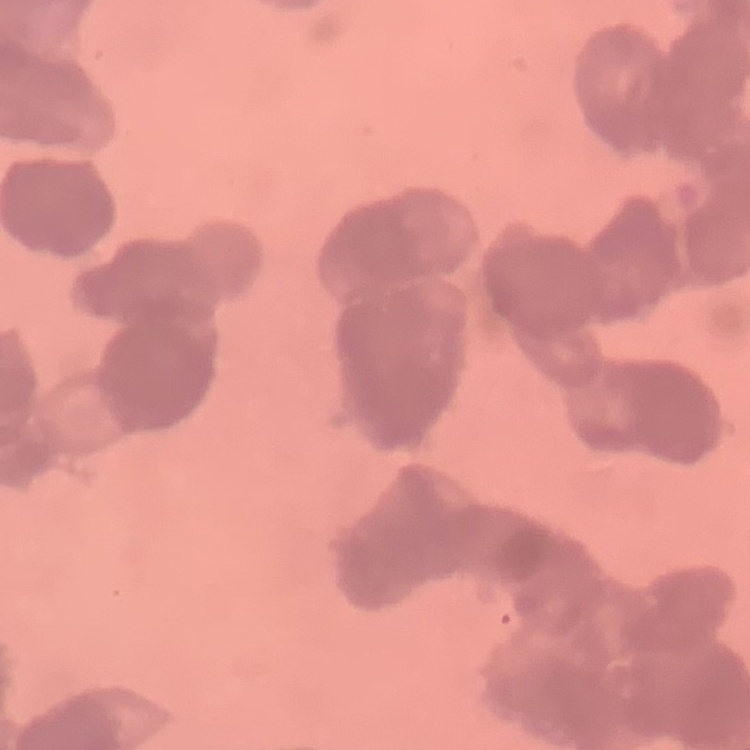

erythrocyte morphology = rouleaux formation
image type = square crop of a larger photomicrograph
stain = Field's or Giemsa
preparation = thin blood film